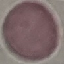

result = no malaria parasites seen
preparation = thin blood film
capture = smartphone camera at the microscope eyepiece
image type = cell patch, automatically extracted from a larger field of view and resized to 64 × 64 pixels
stain = Giemsa